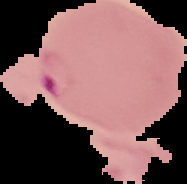

From a thin blood smear. Segmented cell region on a black background. Result: Plasmodium parasites detected. Image is 187×184 pixels.